Report the malaria status of this cell.
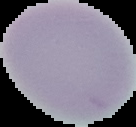
Uninfected.

{
  "preparation": "thin blood film",
  "image_type": "cell region segmented out of the field of view; surrounding area masked to black",
  "image_size": "136×127 pixels"
}